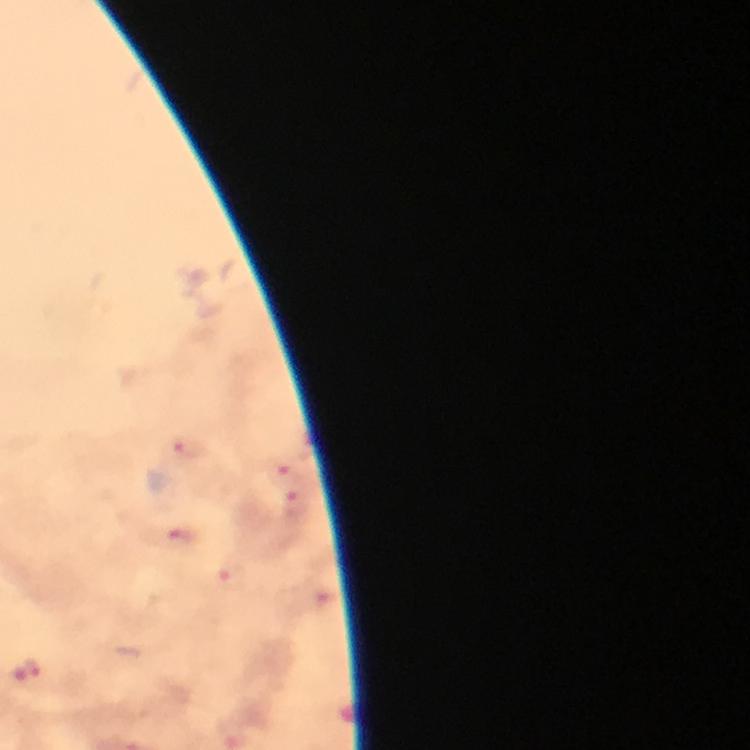
Approximate object centers, in pixels from the top-left corner.
Summary:
  - Plasmodium parasite locations: (x=190, y=448), (x=284, y=473), (x=298, y=504), (x=181, y=542), (x=233, y=579), (x=30, y=673)
  - Context: from a malaria diagnostic workup
  - Image size: 750×750 pixels
  - Cropped from: one field of view
  - Immersion oil: used
  - Magnification: 100x
  - Stain: Giemsa
  - Capture: smartphone mounted on the microscope
  - Preparation: thick blood smear